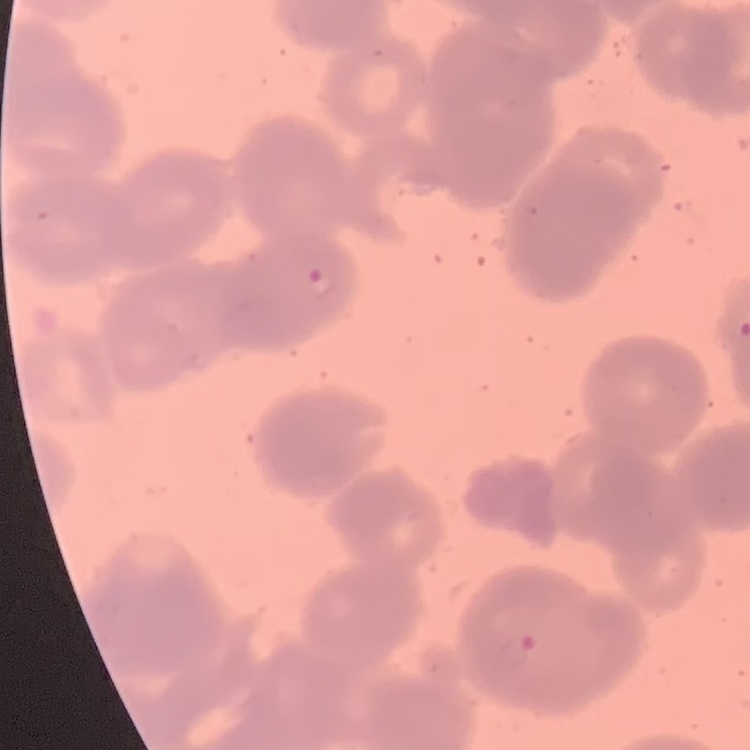
erythrocyte_morphology: rouleaux formation
preparation: thin blood film
image_type: one tile cut from a larger photomicrograph
stain: Field's or Giemsa